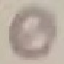 Result: no malaria parasites seen. Cell patch, automatically extracted from a larger field of view and resized to 64 × 64 pixels. Photographed with a smartphone camera at the microscope eyepiece. Giemsa stain. Thin blood film.